Classify this cell by malaria status.
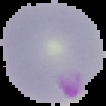
Parasitized.

Summary:
  - Image size: 106×106 pixels
  - Image type: segmented cell region on a black background
  - Preparation: thin blood smear